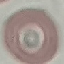

Summary:
  - Result: negative for malaria parasites
  - Stain: Giemsa
  - Image type: cell patch, automatically extracted from a larger field of view and resized to 64 × 64 pixels
  - Capture: smartphone camera at the microscope eyepiece
  - Preparation: thin blood smear